Report the malaria status of this cell.
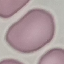
Uninfected.

Summary:
  - Image type: cell patch, automatically extracted from a larger field of view and resized to 64 × 64 pixels
  - Preparation: thin blood smear
  - Capture: smartphone through the microscope eyepiece
  - Stain: Giemsa